Name the parasite shown.
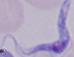
A trypanosome.

1000x magnification. Photomicrograph.